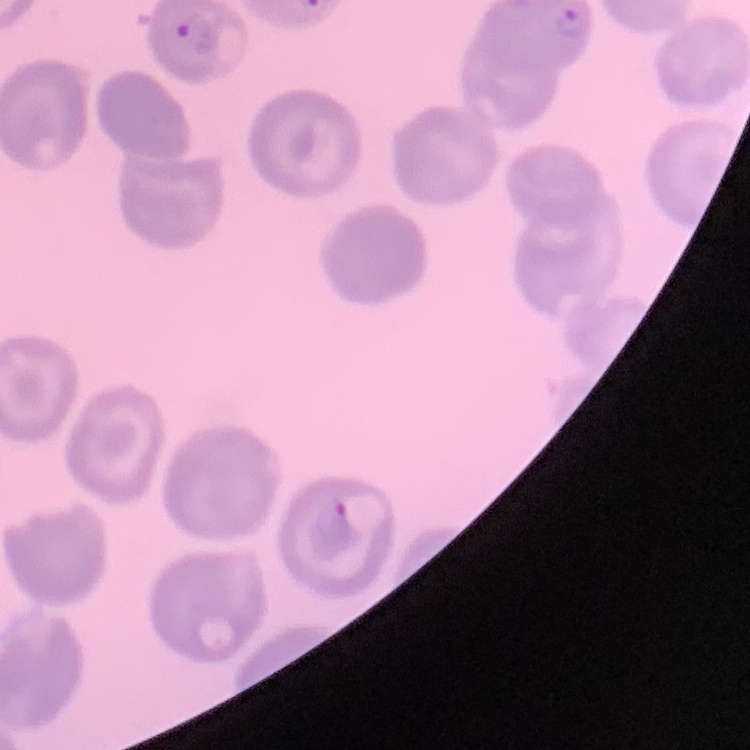
erythrocyte morphology = no rouleaux formation
preparation = thin peripheral smear
image type = one tile cut from a larger photomicrograph
stain = Field's or Giemsa